Assess the morphology of the red blood cells.
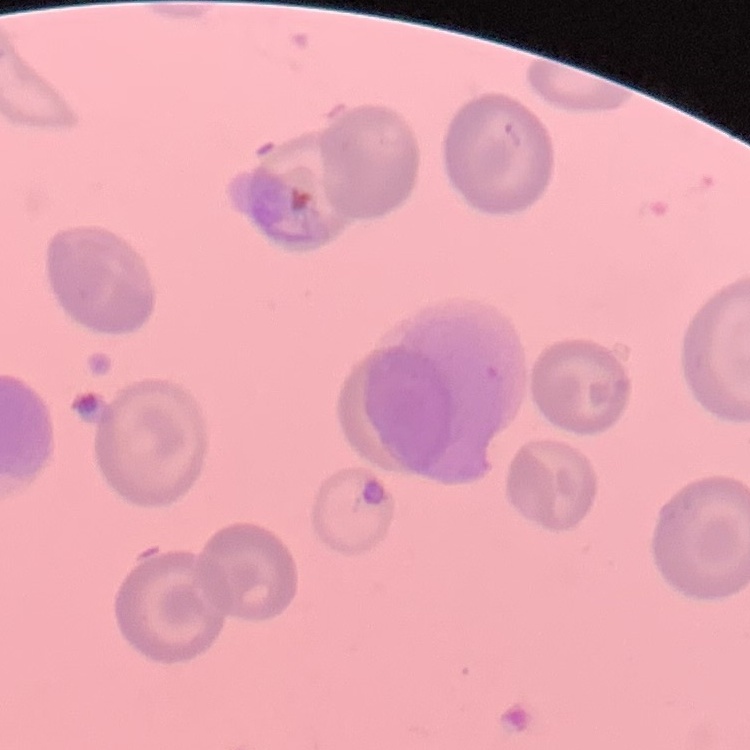

No rouleaux formation.

Summary:
  - Image type: one tile cut from a larger photomicrograph
  - Preparation: thin blood smear
  - Stain: Field's or Giemsa